Outline each Trypanosoma brucei.
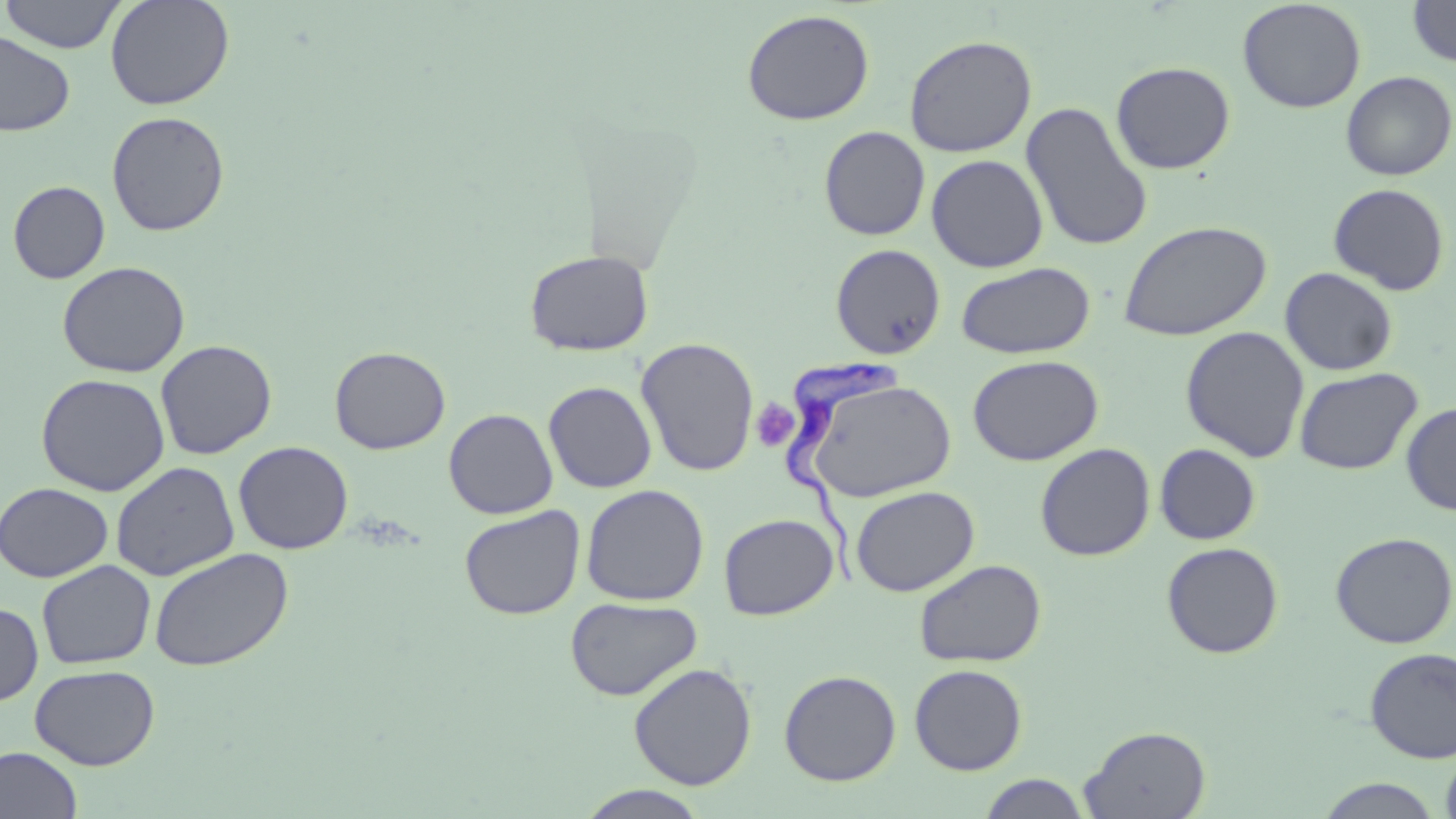

Approximate bounding boxes as named x1/y1/x2/y2 corners in pixels.
Trypanosoma brucei: (x1=783, y1=354, x2=907, y2=592).

Uninfected red blood cell locations: (x1=0, y1=0, x2=127, y2=53), (x1=105, y1=0, x2=235, y2=110), (x1=1237, y1=0, x2=1366, y2=114), (x1=1407, y1=0, x2=1456, y2=68), (x1=742, y1=9, x2=875, y2=126), (x1=0, y1=31, x2=75, y2=136), (x1=903, y1=34, x2=1037, y2=157), (x1=1111, y1=61, x2=1235, y2=174), (x1=1340, y1=71, x2=1455, y2=181), (x1=1021, y1=101, x2=1153, y2=253), (x1=106, y1=111, x2=229, y2=237), (x1=819, y1=125, x2=931, y2=241), (x1=926, y1=154, x2=1049, y2=273), (x1=8, y1=180, x2=111, y2=284), (x1=1328, y1=183, x2=1450, y2=296), (x1=1119, y1=220, x2=1272, y2=341), (x1=830, y1=244, x2=946, y2=359), (x1=524, y1=250, x2=654, y2=357), (x1=57, y1=261, x2=190, y2=378), (x1=956, y1=262, x2=1096, y2=359), (x1=1280, y1=267, x2=1398, y2=376), (x1=1180, y1=325, x2=1310, y2=463), (x1=635, y1=337, x2=759, y2=477), (x1=155, y1=339, x2=277, y2=460), (x1=329, y1=346, x2=451, y2=454), (x1=967, y1=354, x2=1103, y2=466), (x1=1294, y1=367, x2=1422, y2=475), (x1=35, y1=373, x2=170, y2=496), (x1=803, y1=376, x2=957, y2=502), (x1=543, y1=381, x2=657, y2=493), (x1=1401, y1=401, x2=1456, y2=516), (x1=443, y1=408, x2=558, y2=519), (x1=233, y1=440, x2=354, y2=554), (x1=1035, y1=443, x2=1155, y2=561), (x1=1154, y1=443, x2=1261, y2=545), (x1=111, y1=461, x2=240, y2=582), (x1=0, y1=482, x2=114, y2=583), (x1=580, y1=484, x2=709, y2=606), (x1=850, y1=486, x2=979, y2=596), (x1=459, y1=505, x2=585, y2=620), (x1=719, y1=514, x2=839, y2=620), (x1=1330, y1=532, x2=1456, y2=649), (x1=1161, y1=541, x2=1283, y2=658), (x1=149, y1=547, x2=293, y2=672), (x1=914, y1=559, x2=1046, y2=667), (x1=36, y1=560, x2=156, y2=669), (x1=565, y1=596, x2=703, y2=701), (x1=0, y1=601, x2=43, y2=707), (x1=1364, y1=647, x2=1456, y2=763), (x1=628, y1=662, x2=757, y2=790), (x1=909, y1=663, x2=1028, y2=775), (x1=30, y1=664, x2=160, y2=770), (x1=778, y1=669, x2=902, y2=786), (x1=1079, y1=725, x2=1211, y2=819), (x1=1440, y1=744, x2=1456, y2=819), (x1=0, y1=746, x2=83, y2=819), (x1=977, y1=773, x2=1092, y2=818), (x1=1314, y1=778, x2=1445, y2=817), (x1=574, y1=785, x2=713, y2=819). Platelet locations: (x1=750, y1=399, x2=799, y2=453). Slide-level diagnosis: Trypanosoma brucei. Light microscopy. May-Grünwald-Giemsa-stained preparation. Single field of view. Image is 1456×819 pixels. 1000x magnification. Thin blood film.